Assess this cell for malaria.
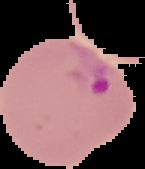
Parasitized.

preparation = thin blood smear
image type = segmented cell region with the area outside set to black
image size = 145×169 pixels